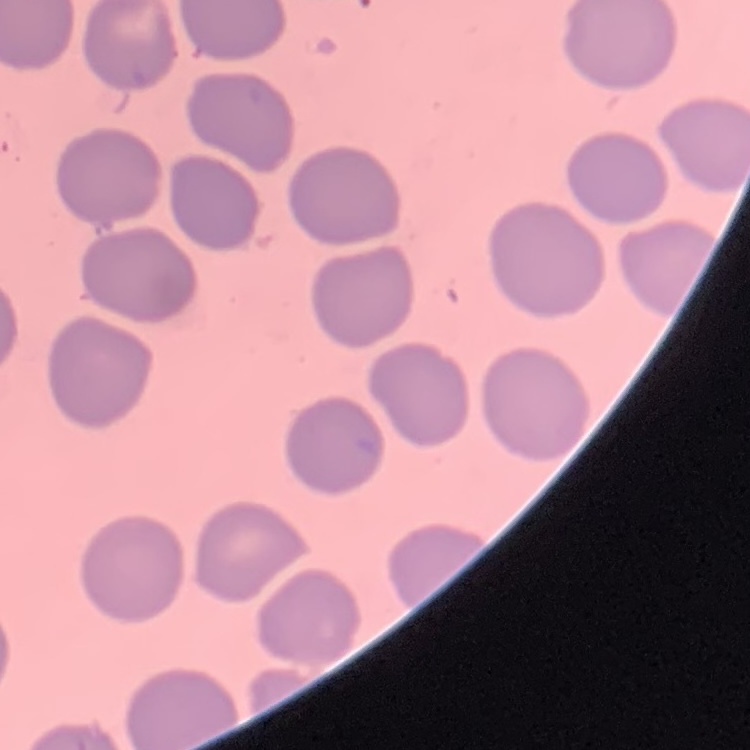

{
  "red_blood_cell_morphology": "no rouleaux formation",
  "stain": "Field's or Giemsa",
  "image_type": "square crop of a larger photomicrograph",
  "preparation": "thin blood smear"
}